Comment on the morphology of the erythrocytes.
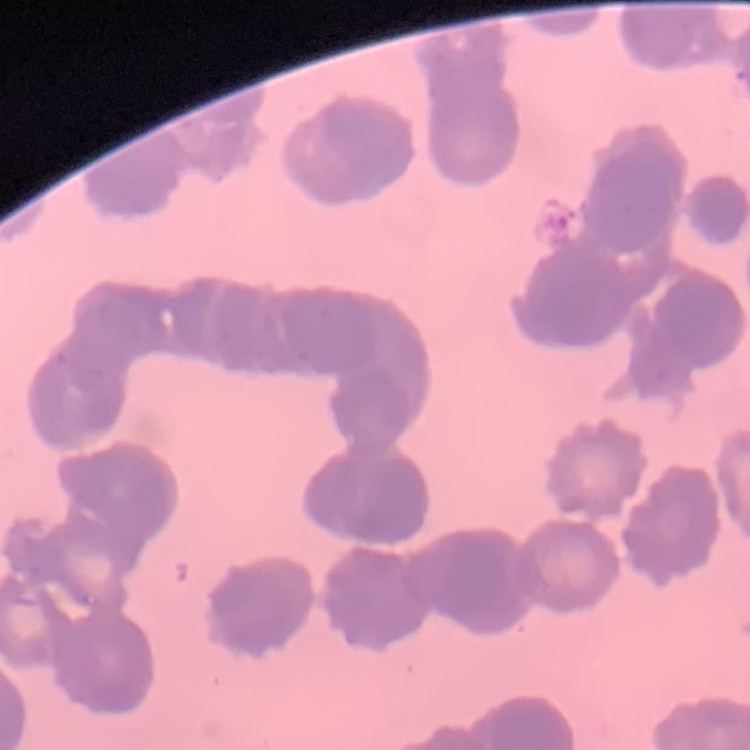
They show rouleaux formation.

Summary:
  - Image type: square crop of a larger photomicrograph
  - Preparation: thin blood smear
  - Stain: Field's or Giemsa